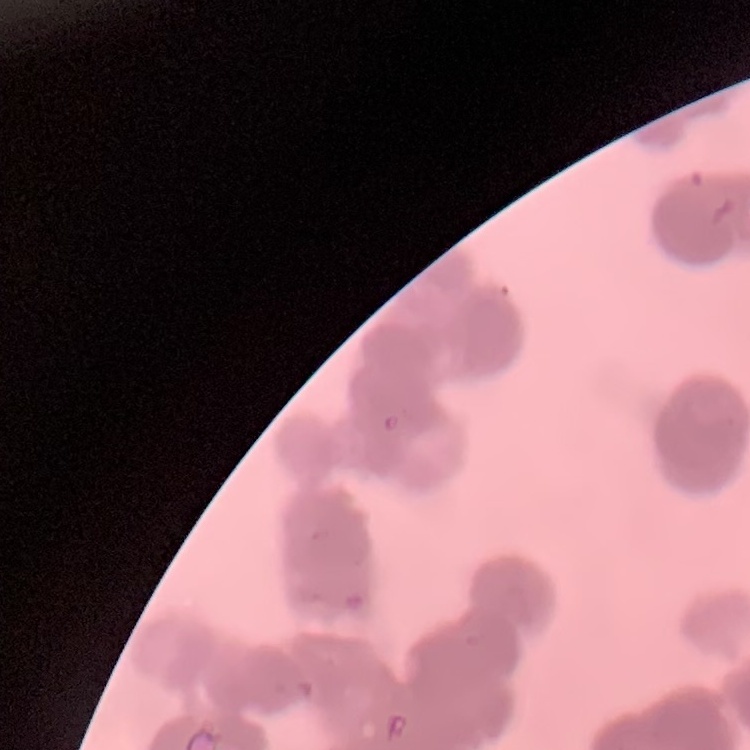

erythrocyte morphology = rouleaux formation
image type = square crop of a larger photomicrograph
preparation = thin blood smear
stain = Field's or Giemsa